Give the extent of all Plasmodium vivax-infected red blood cells.
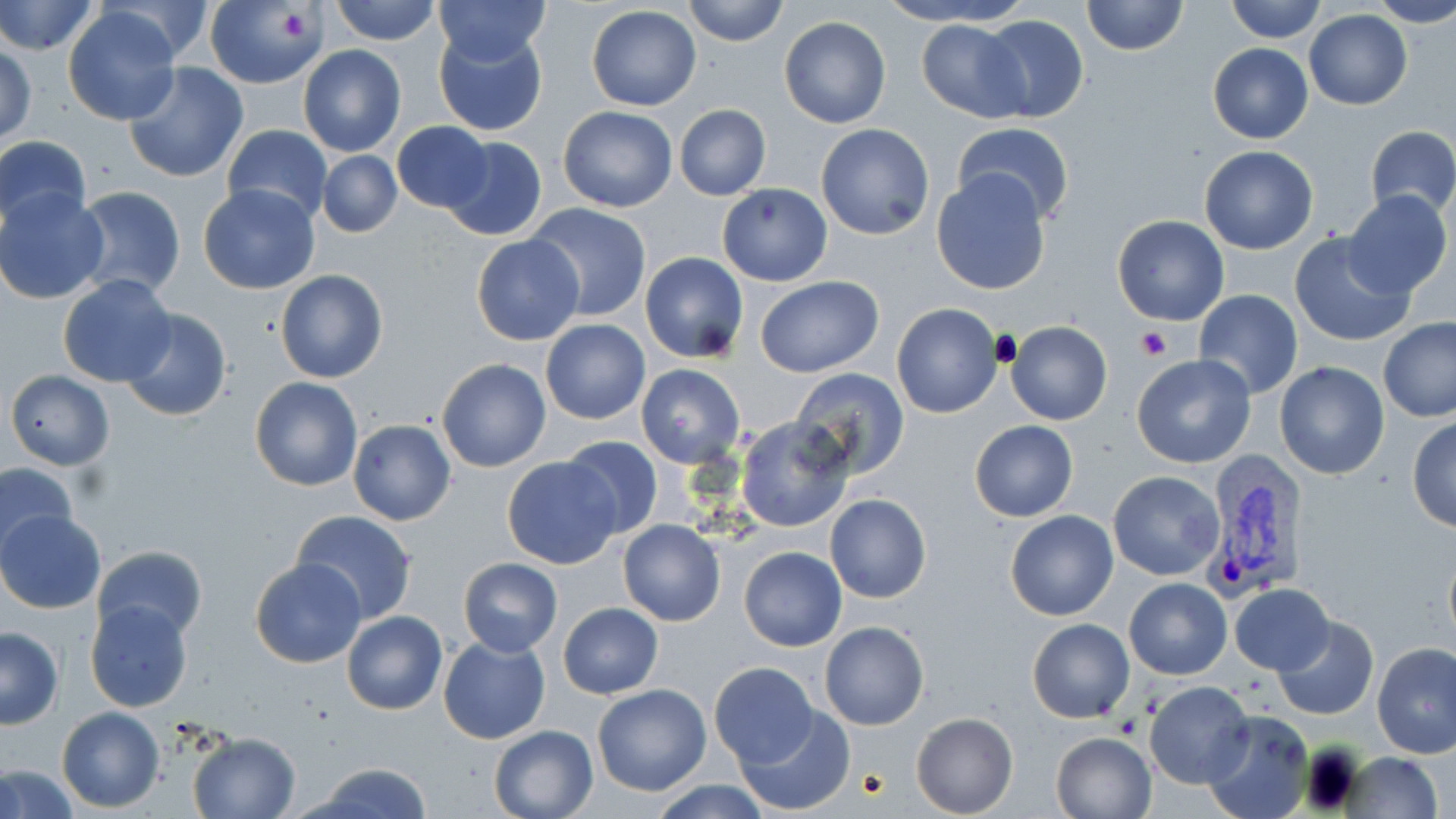
Approximate bounding boxes as (x1,y1)-(x2,y2) corner pairs in pixels.
Plasmodium vivax-infected red blood cells: (1201,458)-(1312,598).

Summary:
  - Uninfected red blood cell locations: (328,0)-(442,45), (434,0)-(550,68), (681,0)-(790,48), (873,0)-(1033,26), (1081,0)-(1186,56), (1227,0)-(1325,42), (1371,0)-(1456,29), (0,1)-(99,56), (100,1)-(219,64), (204,2)-(326,88), (587,5)-(701,112), (62,6)-(182,125), (1304,10)-(1412,109), (980,14)-(1088,122), (779,17)-(891,129), (918,18)-(1027,121), (434,25)-(548,137), (1,43)-(37,147), (1207,43)-(1313,144), (297,45)-(407,158), (123,62)-(250,183), (674,103)-(771,201), (557,105)-(678,212), (393,121)-(493,213), (816,123)-(934,240), (222,124)-(331,223), (952,124)-(1075,225), (1365,126)-(1456,219), (0,135)-(91,235), (440,135)-(547,242), (1199,146)-(1319,254), (317,151)-(402,237), (930,169)-(1053,295), (716,184)-(833,285), (71,185)-(186,300), (198,185)-(321,295), (1,188)-(108,305), (1341,190)-(1452,301), (524,203)-(652,323), (1112,214)-(1229,326), (1287,232)-(1416,347), (471,234)-(585,346), (640,251)-(749,363), (275,270)-(387,384), (58,273)-(176,387), (756,277)-(884,378), (1194,288)-(1303,399), (892,302)-(1002,418), (119,308)-(232,422), (1378,318)-(1456,422), (540,320)-(649,423), (1006,320)-(1112,426), (1132,355)-(1257,470), (437,358)-(551,472), (1274,362)-(1391,480), (636,363)-(746,468), (790,366)-(910,479), (7,369)-(114,470), (250,377)-(362,492), (735,415)-(856,533), (1407,416)-(1456,532), (349,420)-(456,526), (969,420)-(1078,522), (559,436)-(663,540), (502,457)-(622,570), (0,462)-(80,560), (1108,470)-(1224,581), (825,495)-(931,604), (292,508)-(418,625), (0,510)-(105,614), (1005,510)-(1118,621), (618,519)-(726,627), (1443,542)-(1456,652), (93,544)-(208,640), (739,546)-(847,650), (458,557)-(562,656), (251,558)-(367,668), (1124,577)-(1231,679), (1228,583)-(1335,675), (83,599)-(195,713), (558,602)-(665,699), (341,610)-(447,714), (1273,616)-(1379,721), (1026,618)-(1134,722), (820,622)-(929,731), (0,627)-(63,729), (438,636)-(551,745), (1371,641)-(1456,759), (708,662)-(818,766), (591,682)-(713,797), (1143,682)-(1254,788), (734,706)-(854,815), (57,707)-(164,812), (1202,710)-(1315,819), (911,713)-(1018,818), (488,724)-(598,819), (1051,731)-(1158,819), (187,732)-(300,818), (1338,751)-(1445,818), (0,762)-(79,818), (303,762)-(435,819), (646,780)-(773,818)
  - Platelet locations: (278,8)-(317,42), (1135,326)-(1171,361)
  - Slide-level diagnosis: Plasmodium vivax
  - Modality: optical microscopy
  - Magnification: 1000x
  - Image size: 1456×819 pixels
  - Field of view: single
  - Preparation: thin blood film
  - Stain: May-Grünwald-Giemsa